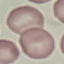

Malaria status: uninfected. Giemsa stain. Photographed with a smartphone camera at the microscope eyepiece. Thin blood film. Automatically extracted cell patch, resized to 64 × 64 pixels.